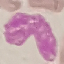

malaria status = uninfected
image type = cell patch, automatically extracted from a larger field of view and resized to 64 × 64 pixels
capture = smartphone camera at the microscope eyepiece
stain = Giemsa
preparation = thin blood film